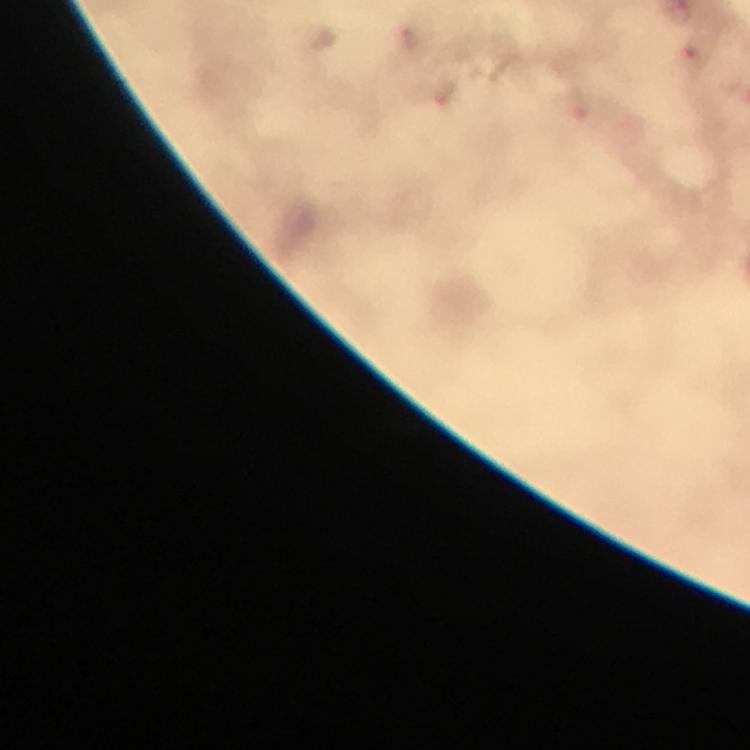

Approximate centers as {x, y} in pixels. Malaria parasite locations: {410, 39}, {444, 92}. Image is 750×750 pixels. Photographed through the microscope with a smartphone camera. A crop from one field of view. From a malaria diagnostic workup. Immersion oil was used. Thick smear. 100x magnification. Giemsa stain.